Evaluate for parasitized red blood cells.
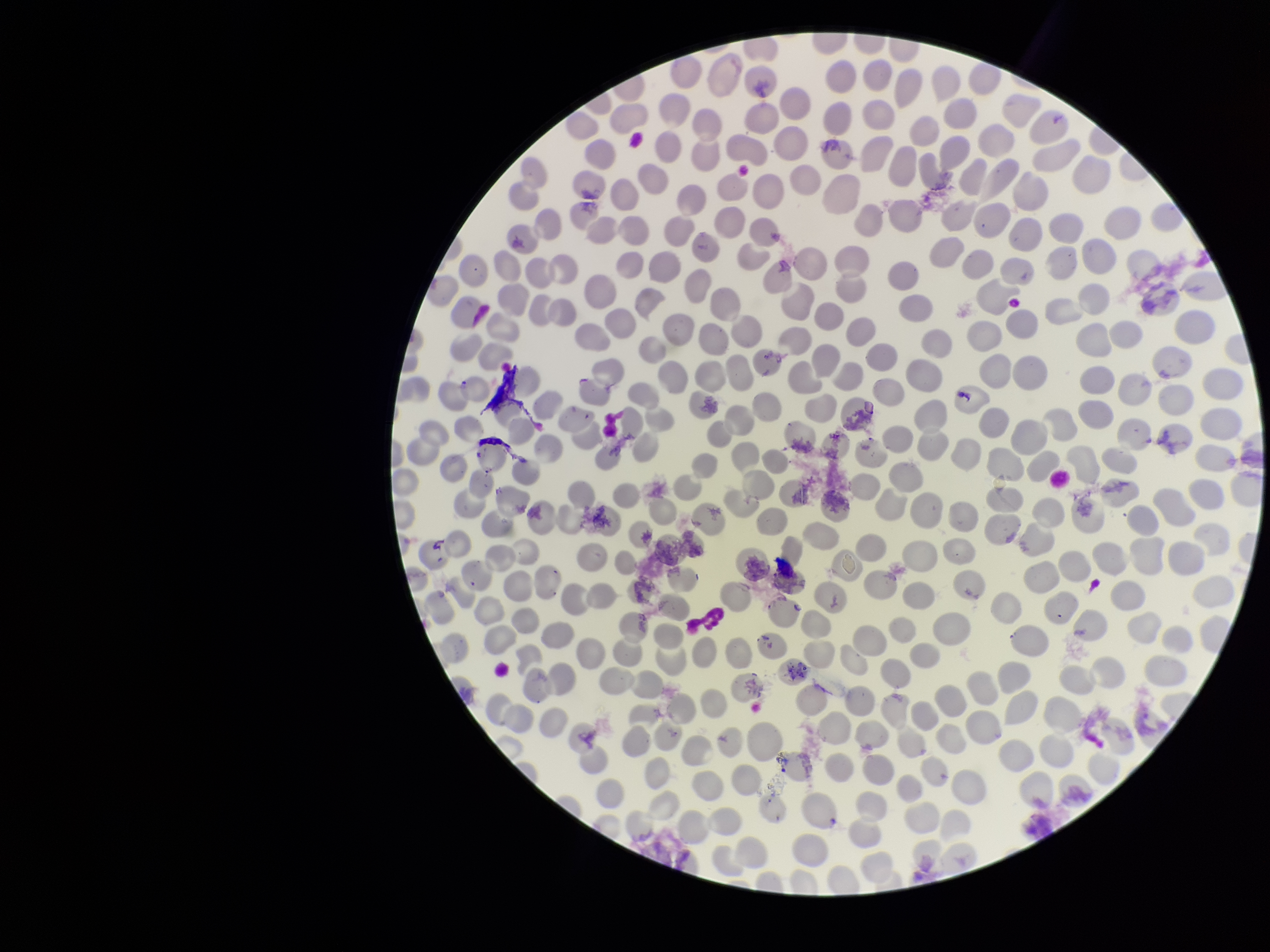
None detected.

Photographed through the microscope eyepiece with a smartphone camera. Preparation: thin blood smear. Parasitized red blood cell count: 0. Patient malaria status: negative. Red blood cell count: 325. Image is 1270×952 pixels. Giemsa stain. One field from this slide.